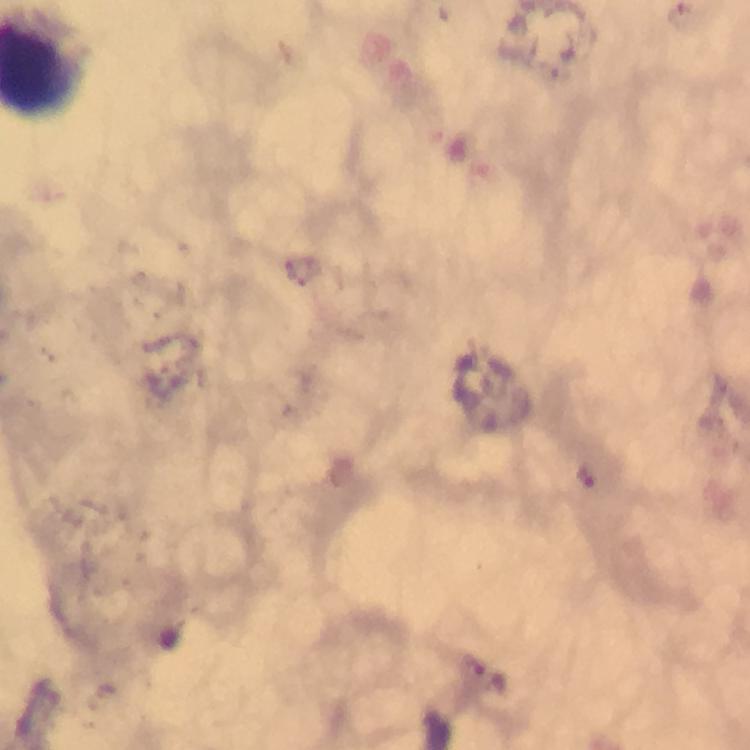
{
  "preparation": "thick smear",
  "stain": "Giemsa",
  "plasmodium_parasite_locations": "approximate centers as [x, y] in pixels: [292, 271], [587, 476], [474, 668]",
  "cropped_from": "one field of view",
  "capture": "smartphone mounted on the microscope",
  "image_size": "750×750 pixels",
  "context": "from a diagnostic examination for malaria",
  "magnification": "100x",
  "immersion_oil": "used"
}